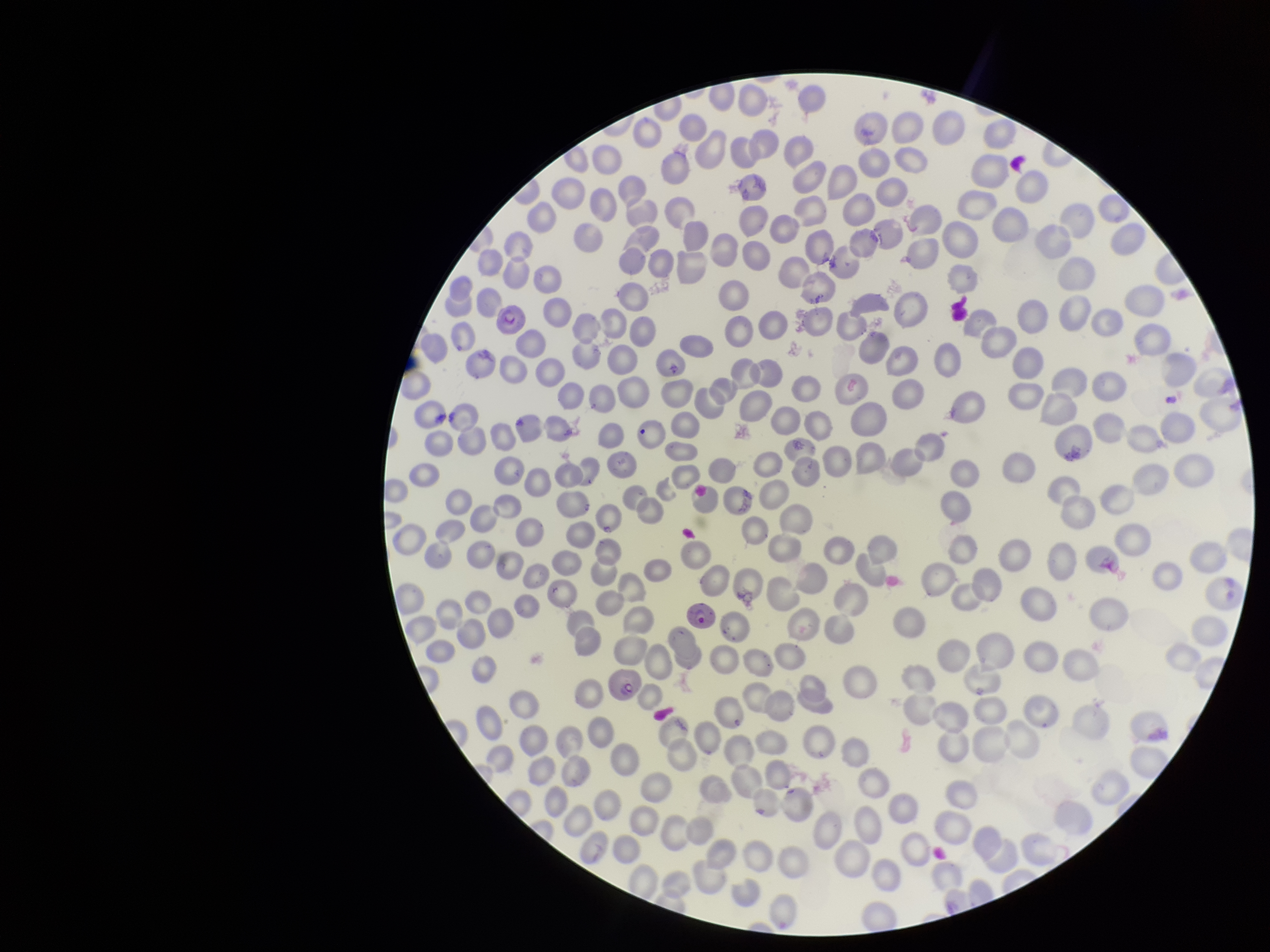

Summary:
  - Image size: 1270×952 pixels
  - Parasitized red blood cell count: 3
  - Stain: Giemsa
  - Preparation: thin
  - Parasitized red blood cells: detected
  - Red blood cell count: 263
  - Patient malaria status: positive
  - Capture: smartphone photograph through the microscope eyepiece
  - Field of view: single
  - Species reported for this patient: Plasmodium falciparum